Report the malaria status of this cell.
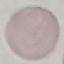
Uninfected.

Acquired by smartphone through the microscope eyepiece. Automatically extracted cell patch, resized to 64 × 64 pixels. Giemsa-stained preparation. Thin smear of blood.